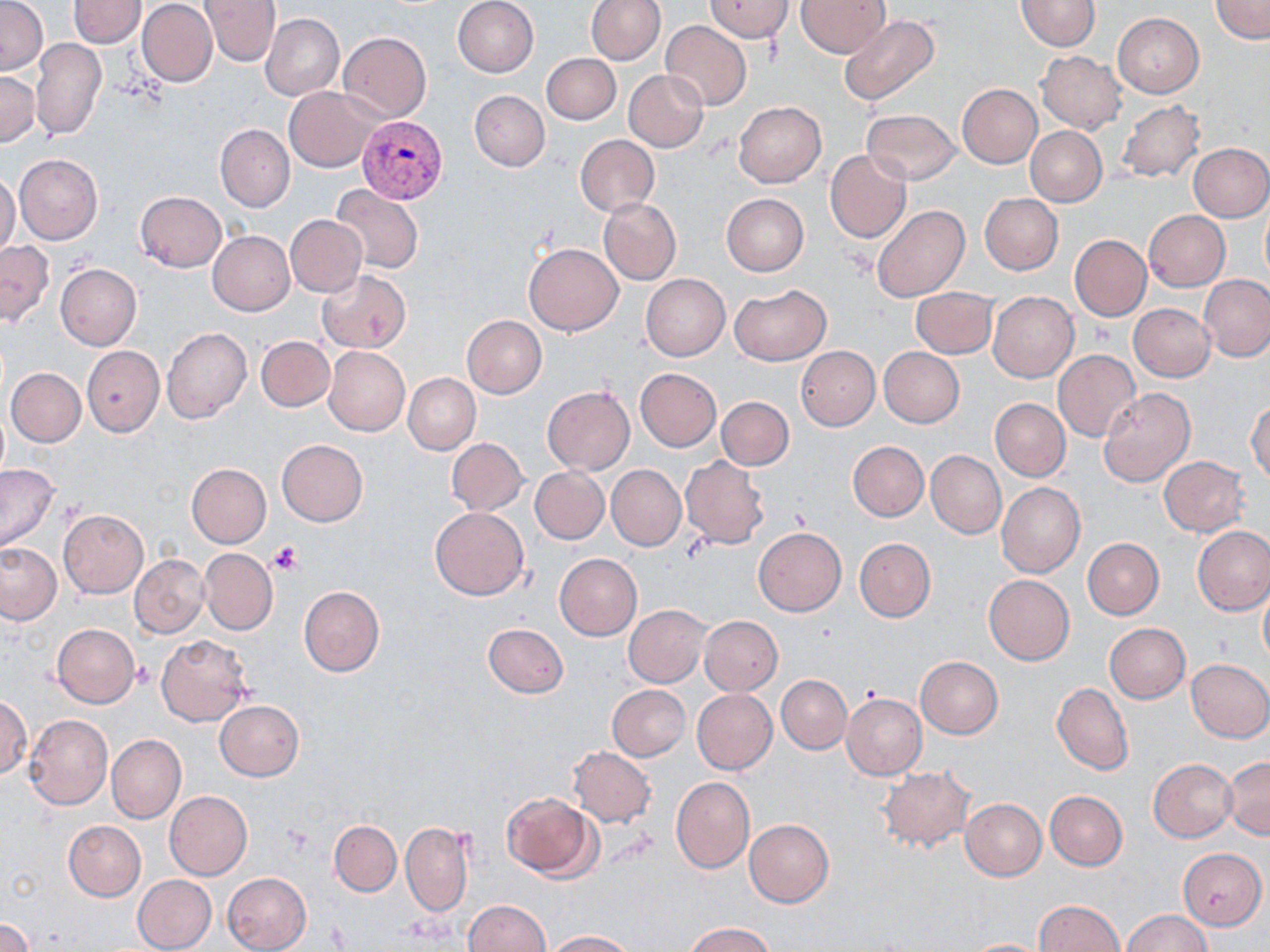
slide_level_diagnosis: Plasmodium vivax
stain: May-Grünwald-Giemsa
image_size: 1270×952 pixels
uninfected_red_blood_cell_locations: 'approximate bounding boxes as (x1,y1)-(x2,y2) corner pairs in pixels: (0,0)-(46,75), (68,0)-(145,49), (200,0)-(280,65), (453,0)-(538,77), (585,0)-(665,65), (796,0)-(891,57), (1209,0)-(1270,43), (137,1)-(218,87), (705,1)-(793,40), (1015,1)-(1100,51), (261,13)-(345,101), (1114,13)-(1204,97), (838,16)-(939,107), (661,21)-(751,111), (339,32)-(431,121), (32,39)-(105,141), (1037,52)-(1127,133), (543,53)-(620,125), (624,70)-(708,151), (0,71)-(40,146), (958,85)-(1042,167), (284,86)-(379,170), (469,90)-(550,172), (734,101)-(825,187), (1117,101)-(1205,183), (862,107)-(960,185), (214,124)-(294,213), (1025,126)-(1107,206), (575,134)-(659,216), (1188,142)-(1270,222), (825,149)-(911,243), (14,153)-(102,244), (0,173)-(20,256), (329,185)-(424,273), (135,191)-(225,271), (979,193)-(1063,275), (722,194)-(808,276), (599,198)-(681,285), (871,206)-(970,302), (1144,211)-(1229,291), (285,215)-(367,297), (208,231)-(294,316), (1069,235)-(1151,322), (0,241)-(54,327), (525,242)-(623,335), (56,264)-(141,350), (316,270)-(411,354), (641,274)-(730,360), (1200,275)-(1270,362), (729,284)-(831,366), (912,288)-(999,358), (988,291)-(1078,381), (1128,304)-(1215,382), (462,316)-(546,399), (162,328)-(252,425), (256,337)-(335,411), (82,345)-(164,436), (796,346)-(879,430), (878,346)-(965,428), (324,347)-(410,436), (1053,350)-(1140,441), (7,359)-(161,440), (5,368)-(85,447), (635,369)-(720,451), (402,373)-(480,455), (543,386)-(634,474), (1098,388)-(1196,488), (717,396)-(793,470), (989,399)-(1069,482), (1247,400)-(1270,485), (446,437)-(528,515), (276,439)-(368,527), (848,441)-(928,522), (926,450)-(1005,538), (680,456)-(770,549), (1159,456)-(1248,536), (186,462)-(271,547), (0,464)-(61,552), (607,466)-(685,549), (530,467)-(609,545), (997,482)-(1085,577), (431,506)-(529,599), (58,510)-(147,598), (1193,525)-(1270,615), (752,527)-(846,616), (854,537)-(935,622), (1083,538)-(1163,619), (0,542)-(62,625), (200,547)-(277,635), (130,554)-(208,638), (554,554)-(642,640), (984,575)-(1075,664), (1258,583)-(1270,667), (298,586)-(385,676), (624,606)-(710,687), (700,616)-(782,694), (50,623)-(140,708), (483,623)-(569,698), (1104,623)-(1190,703), (156,634)-(253,725), (915,656)-(1002,738), (1186,658)-(1270,742), (776,674)-(852,753), (1052,682)-(1133,775), (607,685)-(690,762), (691,689)-(776,775), (842,692)-(927,779), (0,693)-(32,780), (214,700)-(304,781), (25,714)-(113,811), (106,734)-(186,824), (568,747)-(656,827), (1223,756)-(1270,838), (1148,758)-(1238,842), (878,766)-(974,851), (671,776)-(754,873), (1044,790)-(1127,871), (165,791)-(252,881), (500,791)-(599,881), (960,798)-(1046,880), (744,819)-(834,907), (63,820)-(146,900), (329,820)-(401,895), (401,820)-(473,917), (1179,848)-(1268,929), (222,873)-(311,952), (132,875)-(217,952), (462,899)-(550,952), (1035,899)-(1123,951), (1122,910)-(1214,952), (0,917)-(34,952), (686,922)-(774,952), (545,930)-(638,951), (958,938)-(1051,952)'
modality: optical microscopy
plasmodium_vivax_infected_red_blood_cell_locations: 'approximate bounding boxes as (x1,y1)-(x2,y2) corner pairs in pixels: (357,115)-(448,204)'
magnification: 1000x
preparation: thin blood smear
field_of_view: single
platelet_locations: 'approximate bounding boxes as (x1,y1)-(x2,y2) corner pairs in pixels: (267,540)-(304,577), (133,661)-(155,689)'